Locate every blood parasite and identify its species.
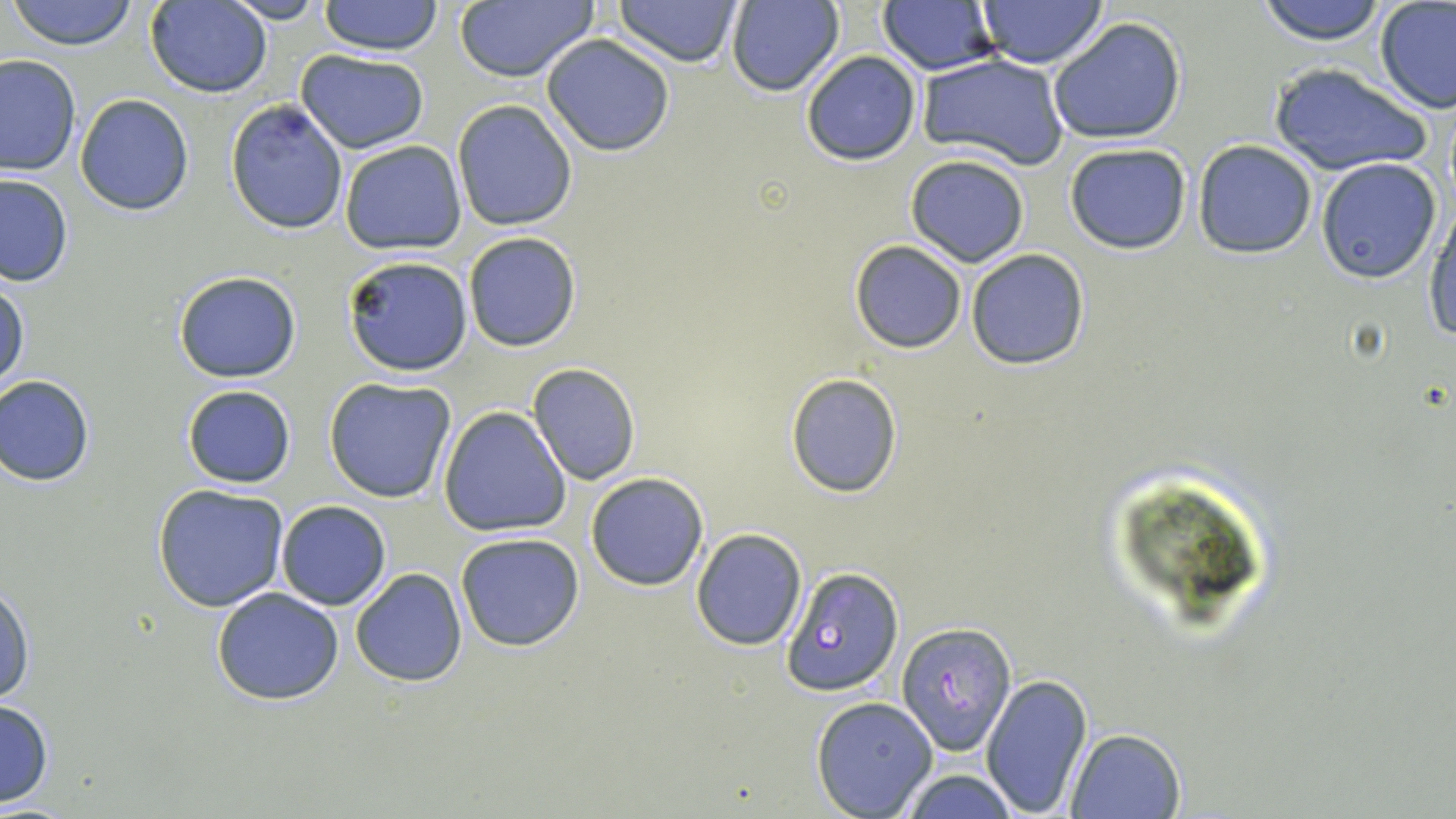
Approximate bounding boxes as (x1, y1, x2, y2) in pixels.
Plasmodium falciparum-infected red blood cells: (782, 567, 904, 696), (898, 622, 1017, 754).
No Plasmodium ovale, Plasmodium malariae, Plasmodium vivax, Babesia divergens, or Trypanosoma brucei observed.

slide-level diagnosis = Plasmodium falciparum
modality = optical microscopy
preparation = thin blood smear
stain = May-Grünwald-Giemsa
field of view = one of a larger specimen
image size = 1456×819 pixels
magnification = 1000x
uninfected red blood cell locations = approximate bounding boxes as (x1, y1, x2, y2) in pixels: (7, 0, 142, 50), (319, 0, 443, 55), (612, 0, 744, 66), (726, 0, 845, 96), (1255, 0, 1388, 46), (145, 1, 273, 99), (220, 1, 330, 24), (879, 1, 999, 74), (974, 1, 1110, 68), (453, 2, 598, 83), (1375, 2, 1456, 112), (1047, 17, 1188, 145), (541, 34, 675, 156), (296, 50, 429, 154), (800, 51, 922, 166), (917, 53, 1069, 170), (0, 54, 81, 178), (1267, 61, 1433, 176), (75, 93, 194, 216), (224, 98, 349, 235), (451, 99, 578, 231), (1192, 139, 1319, 258), (337, 140, 467, 256), (1064, 142, 1194, 256), (905, 153, 1030, 267), (1314, 158, 1441, 283), (0, 174, 73, 287), (1425, 198, 1456, 342), (462, 233, 581, 352), (848, 240, 967, 353), (965, 248, 1091, 371), (342, 255, 472, 375), (174, 272, 302, 384), (0, 275, 29, 396), (527, 363, 641, 485), (1, 374, 95, 487), (785, 374, 903, 498), (324, 377, 458, 503), (181, 385, 297, 489), (438, 406, 571, 537), (586, 471, 710, 593), (151, 483, 291, 613), (275, 500, 392, 610), (690, 529, 808, 650), (454, 532, 585, 652), (349, 568, 469, 686), (0, 578, 35, 706), (210, 588, 343, 706), (981, 673, 1093, 818), (810, 697, 937, 817), (0, 698, 54, 807), (1063, 727, 1186, 818), (898, 767, 1018, 819)